Assess the morphology of the red blood cells.
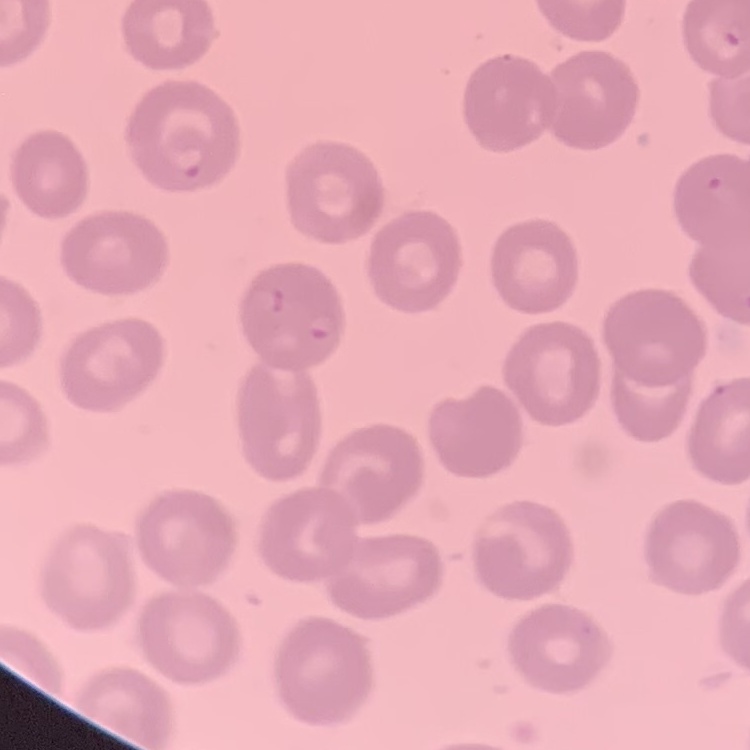

No rouleaux formation.

Summary:
  - Preparation: thin peripheral smear
  - Image type: one tile cut from a larger photomicrograph
  - Stain: Field's or Giemsa